Report the malaria status of this cell.
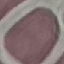
Uninfected.

image type = automatically extracted cell patch, resized to 64 × 64 pixels
capture = smartphone through the microscope eyepiece
preparation = thin blood film
stain = Giemsa